Comment on the morphology of the red blood cells.
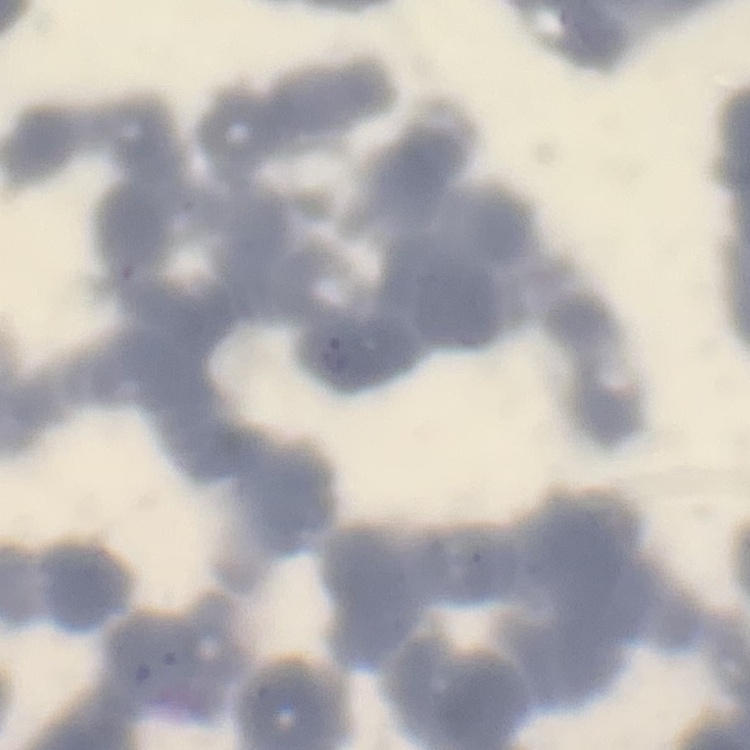

Rouleaux formation.

Thin blood film. Square crop of a larger photomicrograph. Stained with either Field's or Giemsa.